Point out each malaria parasite.
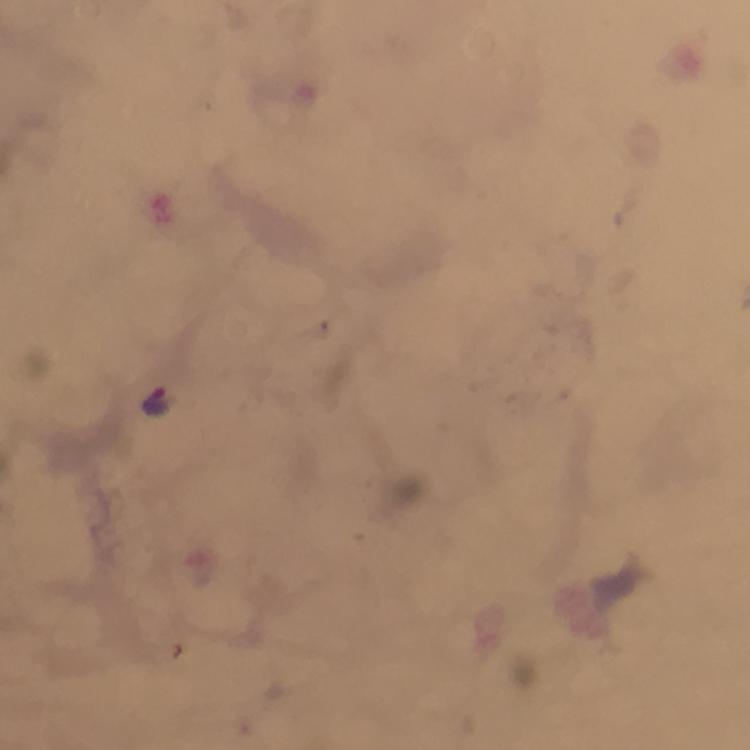

Approximate object centers, in pixels from the top-left corner.
Malaria parasites: (x=157, y=402).

{
  "image_size": "750×750 pixels",
  "immersion_oil": "used",
  "preparation": "thick blood smear",
  "cropped_from": "a single field of view",
  "magnification": "100x",
  "context": "from a diagnostic examination for malaria",
  "capture": "smartphone mounted on the microscope",
  "stain": "Giemsa"
}